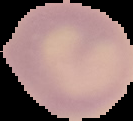

Summary:
  - Image size: 133×121 pixels
  - Preparation: thin blood film
  - Image type: segmented cell region with the area outside set to black
  - Malaria status: uninfected